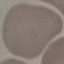
malaria status = uninfected
image type = automatically extracted cell patch, resized to 64 × 64 pixels
preparation = thin blood film
capture = smartphone through the microscope eyepiece
stain = Giemsa